Assess this cell for malaria.
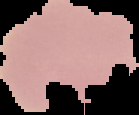

It is uninfected.

Segmented cell region on a black background. From a thin blood film. Image is 139×115 pixels.